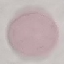
Summary:
  - Result: negative for malaria parasites
  - Capture: smartphone through the microscope eyepiece
  - Stain: Giemsa
  - Image type: automatically extracted cell patch, resized to 64 × 64 pixels
  - Preparation: thin smear